Report the malaria status of this cell.
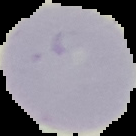
It is uninfected.

image size = 136×136 pixels
preparation = thin blood film
image type = cell region segmented out of the field of view; surrounding area masked to black